Report the malaria status of this cell.
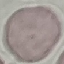
Uninfected.

Summary:
  - Capture: smartphone camera at the microscope eyepiece
  - Image type: automatically extracted cell patch, resized to 64 × 64 pixels
  - Preparation: thin blood smear
  - Stain: Giemsa